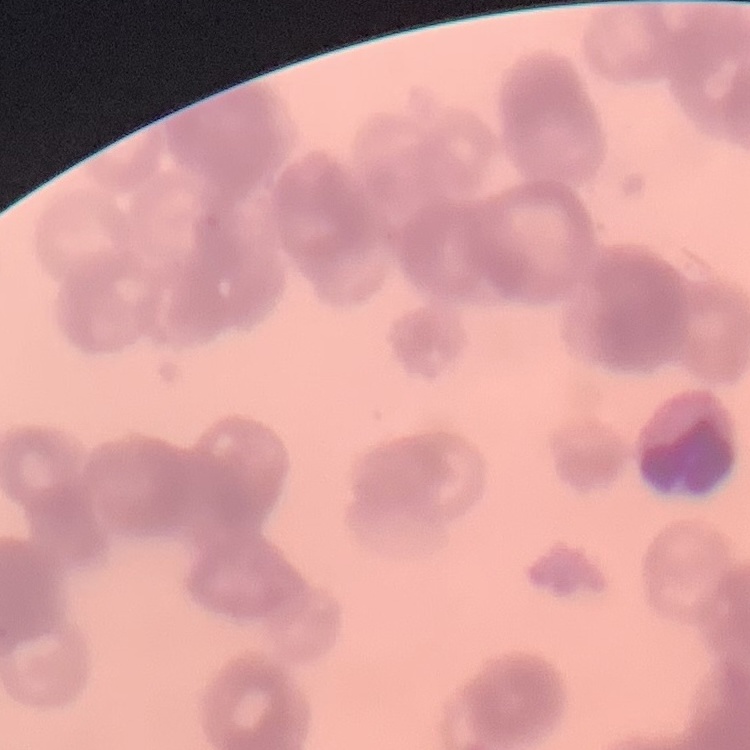

Summary:
  - Red blood cell morphology: rouleaux formation
  - Preparation: thin blood film
  - Stain: Field's or Giemsa
  - Image type: one tile cut from a larger photomicrograph